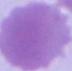

Photomicrograph. An erythrocyte is seen. 1000x magnification.